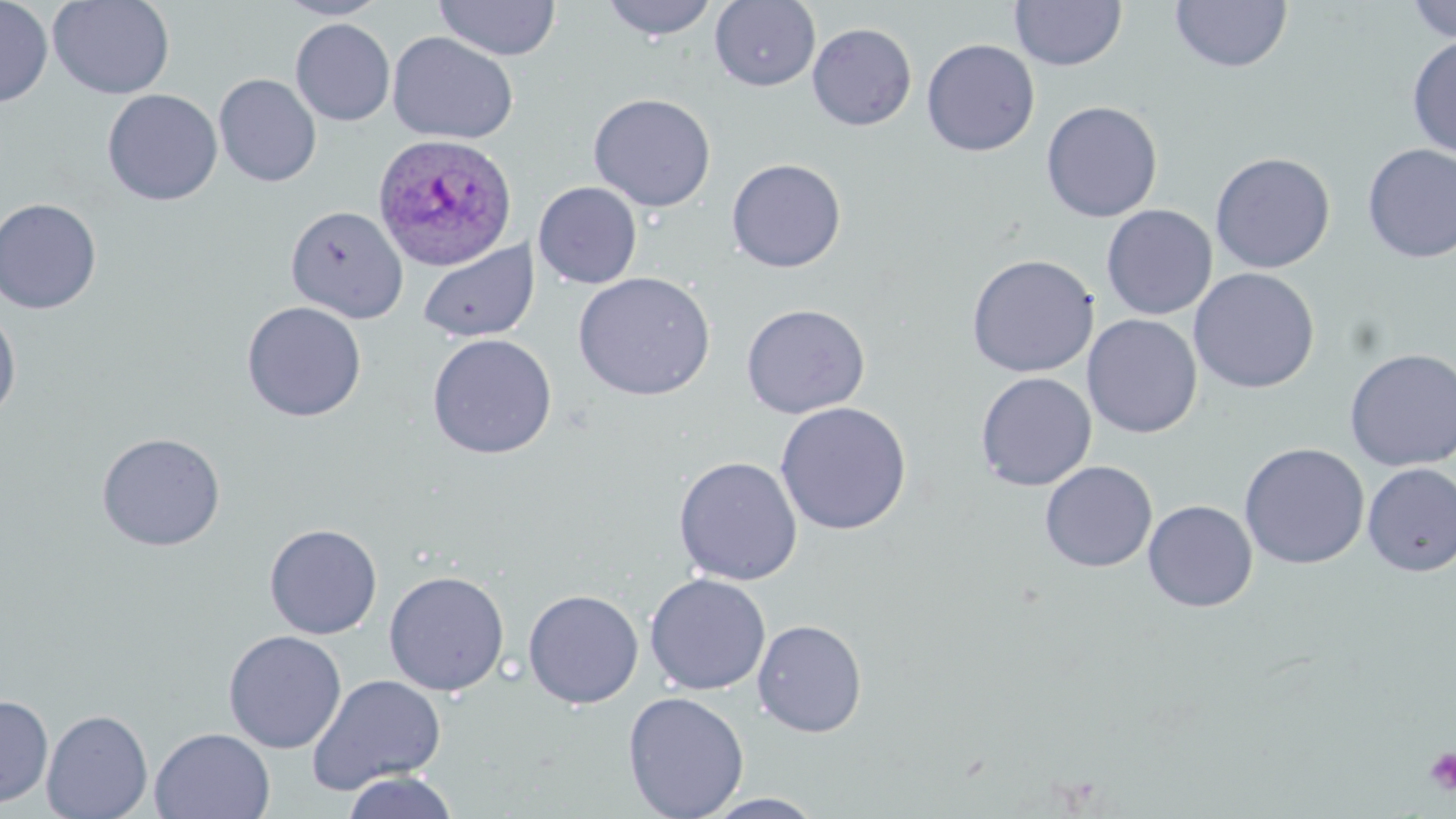
Approximate bounding boxes as (x1, y1, x2, y2) in pixels. Plasmodium ovale-infected red blood cell locations: (371, 133, 519, 271). Uninfected red blood cell locations: (0, 0, 53, 108), (47, 0, 175, 99), (274, 0, 390, 20), (600, 0, 719, 41), (1171, 0, 1292, 74), (1405, 0, 1456, 42), (434, 1, 561, 61), (710, 1, 820, 91), (1010, 1, 1127, 71), (290, 19, 395, 126), (807, 23, 917, 131), (387, 32, 518, 144), (1407, 35, 1456, 159), (921, 39, 1040, 157), (214, 73, 322, 187), (102, 89, 222, 206), (588, 93, 716, 212), (1041, 100, 1163, 223), (1361, 143, 1456, 263), (1210, 152, 1335, 273), (726, 158, 846, 272), (533, 182, 643, 289), (0, 198, 102, 315), (1101, 204, 1217, 320), (285, 205, 408, 323), (418, 241, 539, 343), (965, 254, 1099, 378), (1189, 268, 1320, 394), (572, 272, 716, 401), (242, 301, 367, 421), (741, 303, 870, 418), (0, 306, 22, 424), (1082, 314, 1202, 438), (427, 333, 557, 459), (1344, 348, 1456, 471), (975, 371, 1097, 491), (774, 401, 912, 535), (96, 432, 226, 551), (1239, 442, 1370, 569), (674, 456, 803, 585), (1039, 461, 1157, 573), (1362, 463, 1456, 577), (1143, 501, 1258, 613), (264, 524, 383, 639), (384, 570, 509, 696), (645, 573, 770, 696), (523, 589, 644, 708), (752, 619, 867, 738), (224, 630, 346, 753), (308, 674, 447, 795), (623, 691, 749, 819), (0, 694, 53, 808), (41, 709, 153, 819), (150, 727, 276, 818), (341, 771, 459, 819), (701, 792, 826, 818). Platelet locations: (1423, 747, 1456, 795). Slide-level diagnosis: Plasmodium ovale. May-Grünwald-Giemsa stain. Thin blood film. Captured at 1000x magnification. One field of a larger specimen. Light microscopy. Image is 1456×819 pixels.